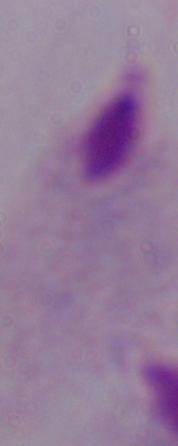

Summary:
  - Magnification: 1000x
  - Modality: photomicrograph
  - Identification: trichomonad